Classify this cell by malaria status.
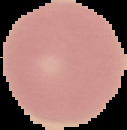

Uninfected.

Image is 127×130 pixels. Segmented cell region on a black background. From a thin blood smear.